Report the malaria status of this cell.
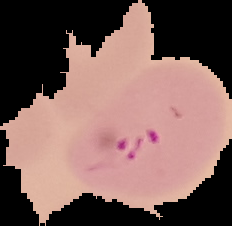

It is parasitized.

preparation = thin blood film
image size = 232×226 pixels
image type = cell region segmented out of the field of view; surrounding area masked to black